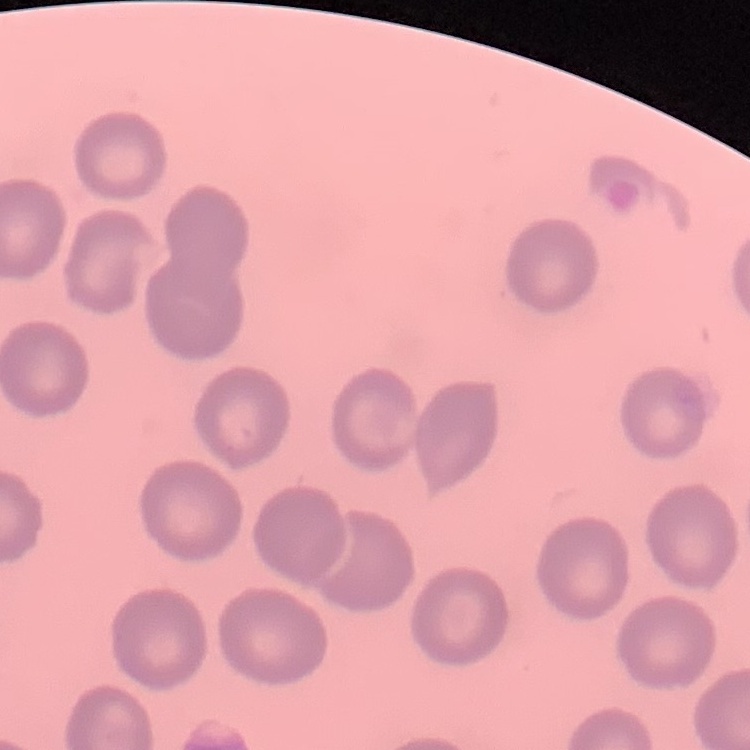

The erythrocytes show no rouleaux formation. Field's or Giemsa stain. Square crop of a larger photomicrograph. Thin blood film.